Report the malaria status of this cell.
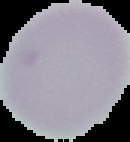
Uninfected.

image size = 130×142 pixels
preparation = thin blood smear
image type = segmented cell region on a black background